Assess the morphology of the red blood cells.
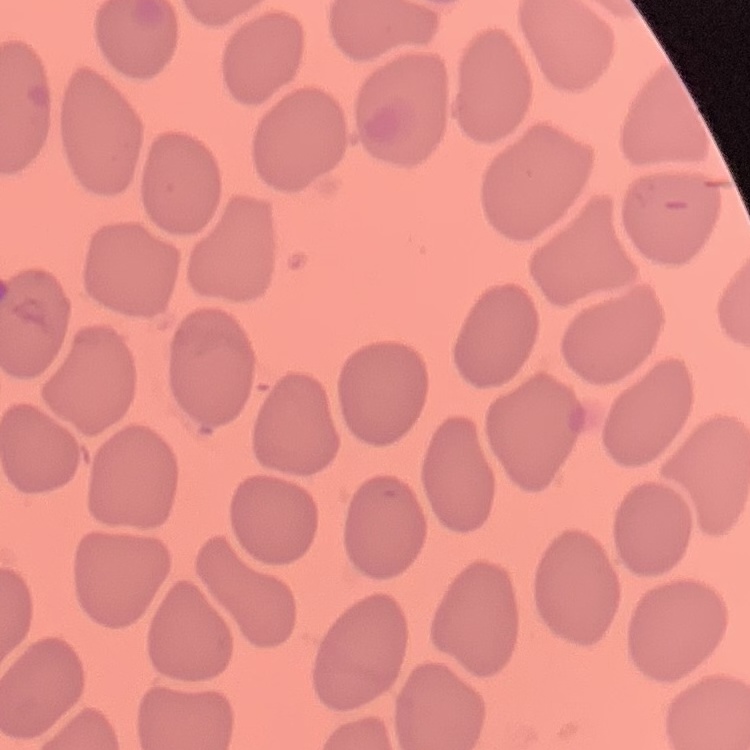
They show no rouleaux formation.

Summary:
  - Preparation: thin blood film
  - Stain: Field's or Giemsa
  - Image type: square crop of a larger photomicrograph